Name the parasite shown.
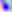
Toxoplasma gondii.

Summary:
  - Magnification: 400x
  - Modality: micrograph